Give the position of every malaria parasite.
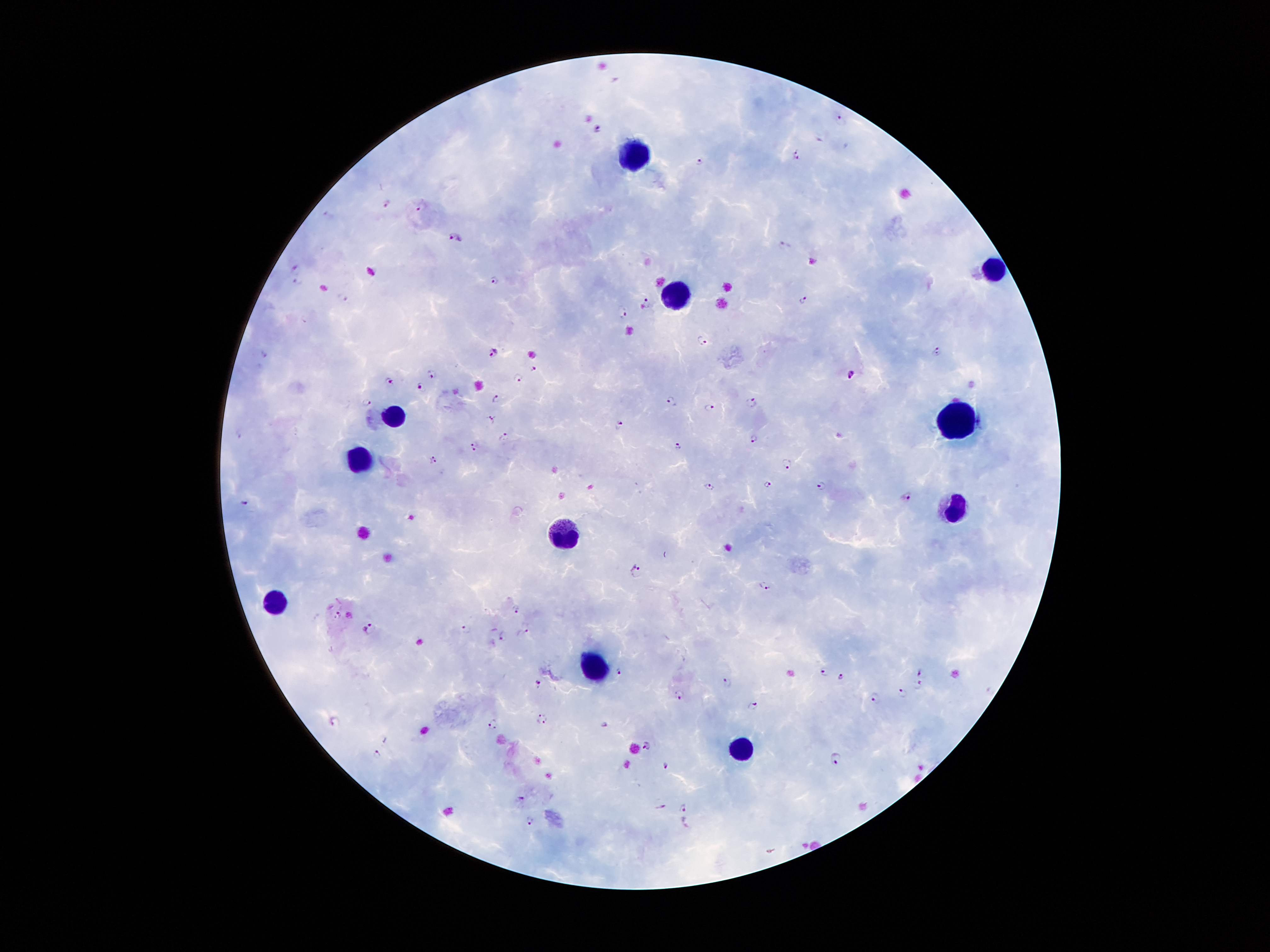
Approximate centers as (x, y) in pixels.
Malaria parasites: (841, 122), (598, 129), (796, 155), (701, 162), (386, 203), (422, 207), (328, 214), (455, 237), (784, 243), (296, 271), (496, 280), (298, 283), (342, 296), (804, 299), (648, 304), (624, 311), (703, 341), (938, 350), (493, 352), (263, 355), (535, 367), (432, 374), (851, 374), (518, 377), (389, 381), (421, 386), (495, 399), (367, 401), (672, 402), (751, 402), (709, 408), (492, 419), (620, 423), (239, 432), (503, 437), (755, 439), (474, 446), (677, 447), (432, 459), (786, 464), (768, 483), (821, 485), (709, 487), (906, 497), (245, 502), (635, 569), (765, 587), (516, 608), (337, 615), (369, 628), (466, 628), (523, 633), (503, 636), (491, 643), (619, 671), (825, 671), (921, 672), (841, 677), (726, 682), (537, 683), (917, 685), (990, 690), (901, 693), (679, 695), (874, 697), (753, 705), (542, 719), (334, 722), (494, 725), (605, 725), (646, 745), (376, 754), (837, 758), (665, 765), (521, 801), (684, 807), (661, 808), (530, 820), (686, 821).

Leukocyte locations: (634, 151), (997, 274), (677, 291), (395, 419), (958, 421), (357, 456), (953, 509), (564, 531), (278, 600), (596, 666), (738, 748). 100x magnification. Patient malaria status: positive for Plasmodium falciparum. Image is 1270×952 pixels. Giemsa-stained preparation. Smartphone photograph taken through the microscope eyepiece. Thick blood smear. Single field of view.